Outline each blood parasite and name the species.
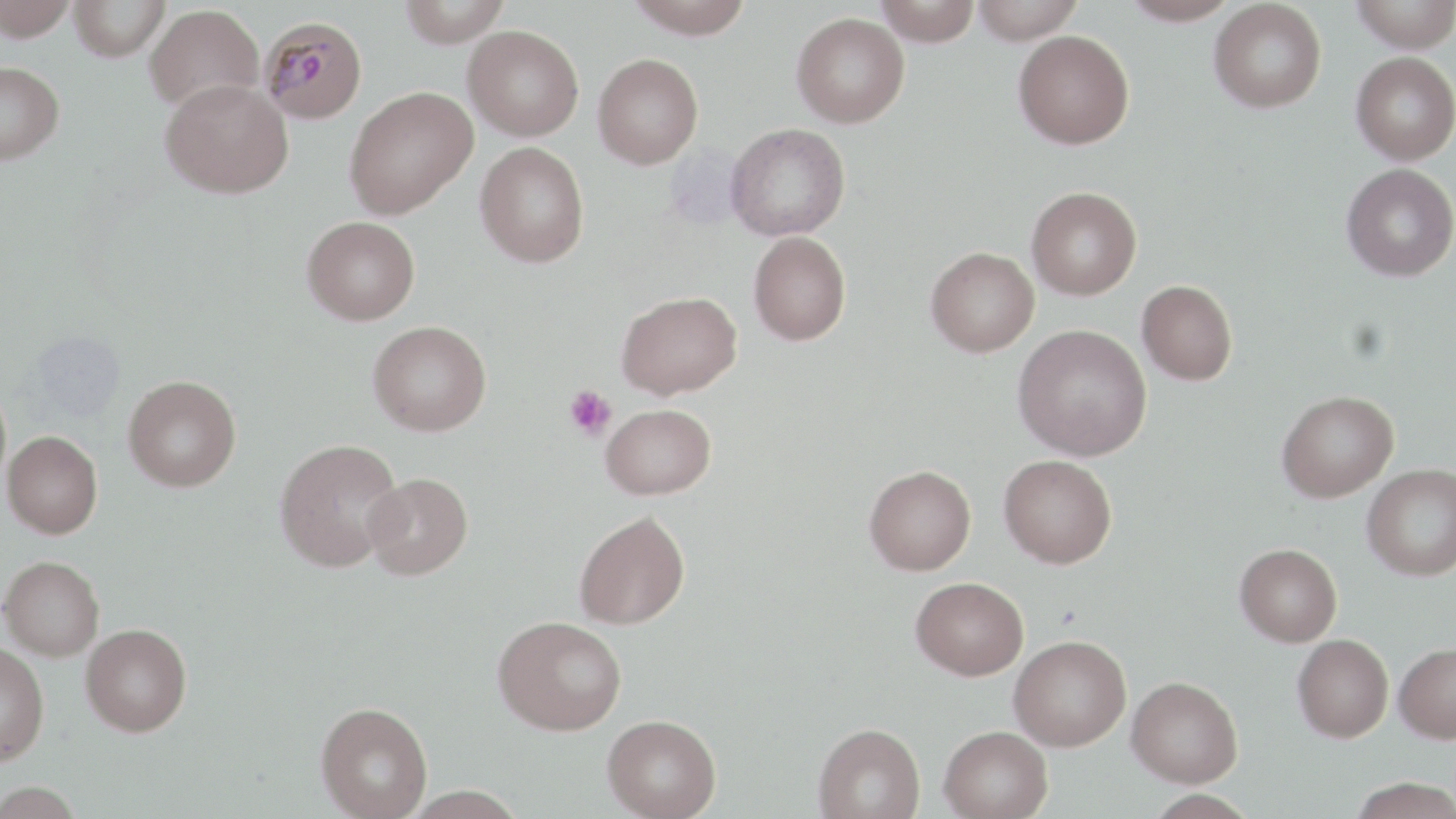
Approximate bounding boxes as named x1/y1/x2/y2 corners in pixels.
Plasmodium malariae-infected red blood cells: (x1=259, y1=15, x2=368, y2=124).
No Plasmodium falciparum, Plasmodium ovale, Plasmodium vivax, Babesia divergens, or Trypanosoma brucei observed.

Summary:
  - Platelet locations: (x1=563, y1=386, x2=617, y2=440)
  - Uninfected red blood cell locations: (x1=0, y1=0, x2=80, y2=41), (x1=68, y1=0, x2=170, y2=61), (x1=398, y1=0, x2=512, y2=47), (x1=624, y1=0, x2=755, y2=39), (x1=874, y1=0, x2=982, y2=46), (x1=971, y1=0, x2=1084, y2=43), (x1=1122, y1=0, x2=1239, y2=26), (x1=1209, y1=0, x2=1327, y2=113), (x1=1350, y1=0, x2=1456, y2=53), (x1=144, y1=4, x2=264, y2=112), (x1=791, y1=12, x2=910, y2=127), (x1=463, y1=25, x2=584, y2=140), (x1=1013, y1=30, x2=1135, y2=149), (x1=1351, y1=51, x2=1456, y2=165), (x1=592, y1=53, x2=703, y2=169), (x1=0, y1=61, x2=64, y2=165), (x1=160, y1=78, x2=293, y2=199), (x1=344, y1=87, x2=478, y2=219), (x1=727, y1=123, x2=851, y2=241), (x1=475, y1=141, x2=590, y2=268), (x1=1341, y1=163, x2=1456, y2=282), (x1=1027, y1=186, x2=1142, y2=299), (x1=302, y1=216, x2=420, y2=325), (x1=749, y1=231, x2=851, y2=346), (x1=925, y1=246, x2=1039, y2=357), (x1=1137, y1=280, x2=1238, y2=385), (x1=617, y1=290, x2=742, y2=399), (x1=368, y1=321, x2=492, y2=436), (x1=1013, y1=323, x2=1152, y2=462), (x1=123, y1=375, x2=241, y2=492), (x1=1277, y1=390, x2=1399, y2=502), (x1=601, y1=403, x2=716, y2=499), (x1=2, y1=431, x2=102, y2=538), (x1=274, y1=438, x2=404, y2=572), (x1=998, y1=454, x2=1117, y2=568), (x1=864, y1=464, x2=976, y2=575), (x1=1362, y1=464, x2=1456, y2=580), (x1=363, y1=472, x2=473, y2=579), (x1=574, y1=510, x2=690, y2=629), (x1=1235, y1=544, x2=1342, y2=646), (x1=0, y1=555, x2=104, y2=660), (x1=911, y1=576, x2=1028, y2=680), (x1=493, y1=615, x2=626, y2=735), (x1=81, y1=623, x2=192, y2=736), (x1=1009, y1=634, x2=1131, y2=750), (x1=1292, y1=634, x2=1394, y2=741), (x1=0, y1=642, x2=49, y2=765), (x1=1393, y1=642, x2=1456, y2=743), (x1=1127, y1=675, x2=1243, y2=787), (x1=315, y1=702, x2=433, y2=819), (x1=602, y1=714, x2=721, y2=819), (x1=813, y1=722, x2=925, y2=818), (x1=939, y1=725, x2=1053, y2=819), (x1=1349, y1=777, x2=1456, y2=819), (x1=0, y1=781, x2=86, y2=818)
  - Slide-level diagnosis: Plasmodium malariae
  - Modality: light microscopy
  - Preparation: thin blood film
  - Stain: May-Grünwald-Giemsa
  - Field of view: one of a larger specimen
  - Image size: 1456×819 pixels
  - Magnification: 1000x